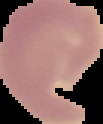
Cell region segmented out of the field of view; the surrounding area is masked to black. From a thin blood smear. Result: negative for Plasmodium parasites. Image is 103×124 pixels.